Locate and identify every blood parasite.
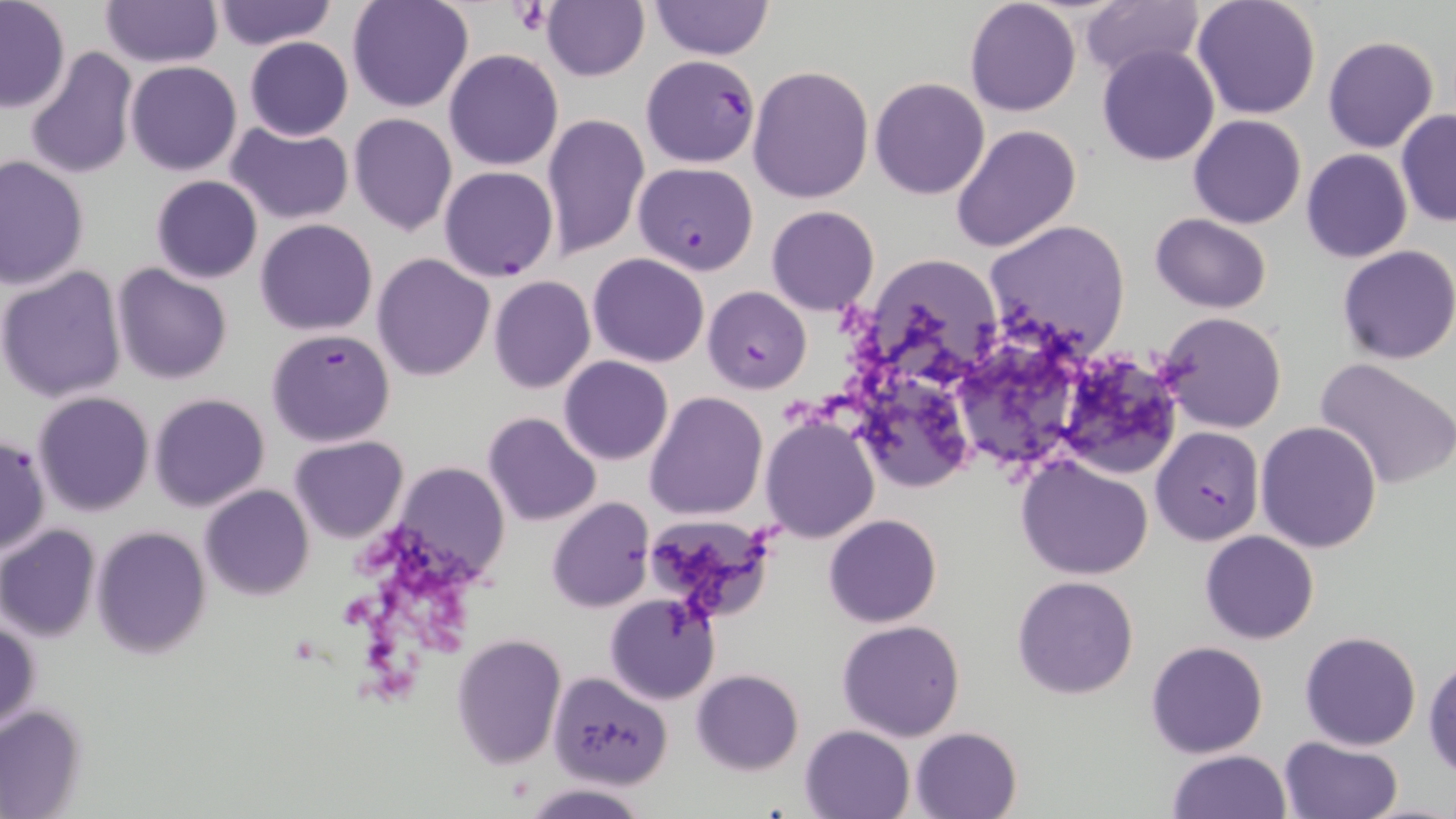
Approximate bounding boxes as (x1, y1, x2, y2) in pixels.
Plasmodium falciparum-infected red blood cells: (640, 56, 762, 168), (632, 162, 759, 275), (439, 166, 558, 282), (703, 285, 811, 394), (266, 328, 396, 447), (1150, 427, 1265, 545), (1, 434, 47, 558).
No Plasmodium ovale, Plasmodium malariae, Plasmodium vivax, Babesia divergens, or Trypanosoma brucei observed.

{
  "slide_level_diagnosis": "Plasmodium falciparum",
  "uninfected_red_blood_cell_locations": "approximate bounding boxes as (x1, y1, x2, y2) in pixels: (99, 0, 220, 67), (650, 0, 774, 59), (966, 0, 1080, 117), (1192, 0, 1322, 121), (210, 1, 338, 50), (346, 1, 475, 114), (0, 2, 71, 112), (542, 2, 648, 81), (1082, 3, 1201, 80), (380, 17, 518, 146), (243, 36, 353, 141), (1323, 36, 1438, 154), (1098, 45, 1220, 165), (24, 47, 138, 181), (443, 49, 563, 170), (124, 62, 242, 176), (748, 65, 873, 202), (870, 77, 990, 200), (1396, 109, 1456, 226), (542, 111, 649, 261), (349, 112, 457, 236), (1188, 114, 1306, 228), (226, 122, 354, 225), (950, 122, 1080, 253), (1300, 148, 1412, 263), (1, 155, 88, 289), (150, 175, 263, 283), (766, 206, 879, 316), (1150, 212, 1272, 312), (255, 219, 378, 336), (985, 219, 1132, 356), (1337, 244, 1456, 365), (372, 253, 495, 380), (588, 254, 709, 367), (874, 255, 1004, 380), (0, 264, 129, 403), (113, 264, 233, 385), (489, 275, 595, 394), (1155, 312, 1289, 433), (1049, 347, 1182, 481), (973, 348, 1076, 477), (559, 356, 672, 465), (1315, 356, 1456, 491), (869, 385, 985, 499), (33, 390, 156, 516), (644, 390, 767, 521), (148, 393, 270, 511), (483, 412, 600, 526), (760, 417, 879, 543), (1256, 421, 1383, 554), (289, 436, 409, 543), (1016, 455, 1154, 580), (391, 461, 510, 583), (200, 484, 313, 600), (547, 497, 655, 612), (823, 513, 942, 627), (0, 525, 101, 641), (93, 527, 212, 659), (1199, 530, 1321, 644), (1013, 574, 1140, 699), (605, 593, 721, 705), (1, 618, 40, 734), (837, 618, 966, 741), (1300, 631, 1421, 750), (451, 634, 566, 772), (1146, 640, 1269, 758), (1424, 654, 1456, 777), (691, 669, 804, 775), (548, 670, 673, 787), (0, 704, 87, 818), (800, 725, 914, 818), (910, 726, 1022, 818), (1279, 736, 1403, 819), (1168, 748, 1291, 819), (521, 781, 650, 818)",
  "field_of_view": "single",
  "preparation": "thin blood film",
  "platelet_locations": "approximate bounding boxes as (x1, y1, x2, y2) in pixels: (511, 2, 553, 37)",
  "magnification": "1000x",
  "image_size": "1456×819 pixels",
  "modality": "optical microscopy",
  "stain": "May-Grünwald-Giemsa"
}